Locate every blood parasite and identify its species.
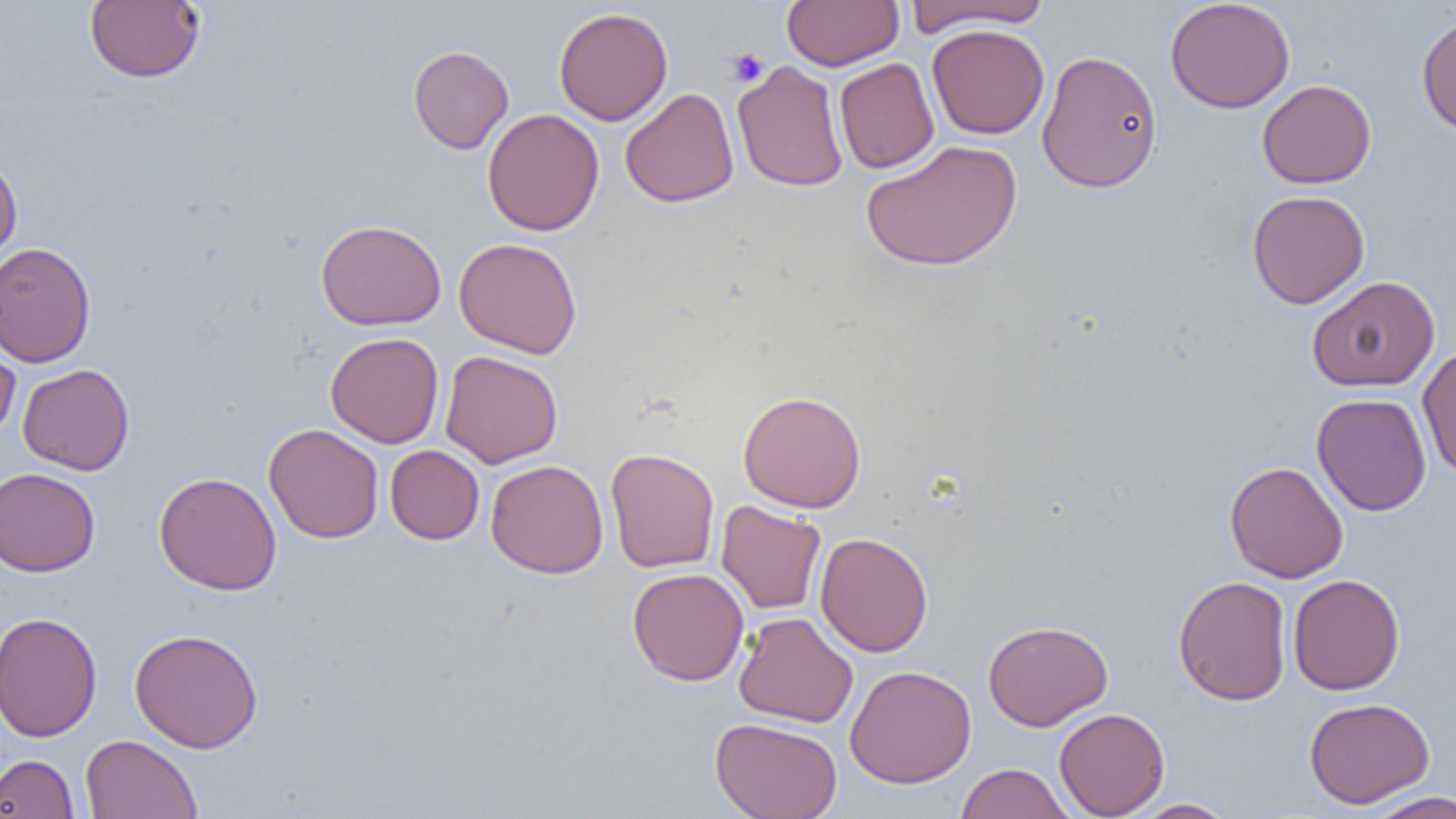
No blood parasites observed.

slide-level diagnosis = negative for blood parasites
preparation = thin blood smear
platelet locations = approximate bounding boxes as named x1/y1/x2/y2 corners in pixels: (x1=726, y1=47, x2=768, y2=86)
image size = 1456×819 pixels
magnification = 1000x
modality = light microscopy
uninfected red blood cell locations = approximate bounding boxes as named x1/y1/x2/y2 corners in pixels: (x1=84, y1=0, x2=204, y2=83), (x1=781, y1=0, x2=904, y2=71), (x1=903, y1=0, x2=1052, y2=35), (x1=1165, y1=0, x2=1296, y2=114), (x1=553, y1=7, x2=673, y2=126), (x1=1416, y1=13, x2=1456, y2=137), (x1=926, y1=24, x2=1049, y2=139), (x1=408, y1=45, x2=514, y2=154), (x1=1036, y1=49, x2=1163, y2=193), (x1=834, y1=58, x2=940, y2=174), (x1=732, y1=60, x2=849, y2=192), (x1=1257, y1=79, x2=1376, y2=188), (x1=620, y1=87, x2=739, y2=207), (x1=482, y1=108, x2=604, y2=237), (x1=860, y1=140, x2=1022, y2=272), (x1=0, y1=153, x2=22, y2=270), (x1=1247, y1=190, x2=1369, y2=309), (x1=316, y1=219, x2=446, y2=331), (x1=454, y1=237, x2=582, y2=359), (x1=0, y1=241, x2=97, y2=367), (x1=1307, y1=275, x2=1440, y2=392), (x1=0, y1=331, x2=21, y2=444), (x1=325, y1=332, x2=444, y2=448), (x1=1417, y1=344, x2=1456, y2=478), (x1=440, y1=350, x2=563, y2=468), (x1=17, y1=363, x2=135, y2=475), (x1=738, y1=390, x2=867, y2=513), (x1=1312, y1=393, x2=1432, y2=517), (x1=264, y1=423, x2=384, y2=544), (x1=385, y1=445, x2=484, y2=545), (x1=605, y1=447, x2=720, y2=573), (x1=486, y1=459, x2=608, y2=578), (x1=1224, y1=461, x2=1349, y2=583), (x1=0, y1=467, x2=101, y2=577), (x1=154, y1=472, x2=282, y2=596), (x1=715, y1=500, x2=826, y2=615), (x1=815, y1=532, x2=933, y2=657), (x1=627, y1=568, x2=749, y2=686), (x1=1287, y1=573, x2=1405, y2=695), (x1=1174, y1=575, x2=1292, y2=706), (x1=0, y1=611, x2=102, y2=742), (x1=734, y1=612, x2=858, y2=728), (x1=983, y1=620, x2=1113, y2=731), (x1=129, y1=628, x2=264, y2=753), (x1=845, y1=665, x2=976, y2=789), (x1=1304, y1=697, x2=1435, y2=808), (x1=1054, y1=708, x2=1170, y2=817), (x1=710, y1=717, x2=843, y2=819), (x1=80, y1=734, x2=202, y2=819), (x1=0, y1=754, x2=80, y2=818), (x1=955, y1=762, x2=1075, y2=819), (x1=1364, y1=790, x2=1456, y2=818), (x1=1128, y1=798, x2=1240, y2=818)
field of view = one of a larger specimen